Assess this cell for malaria.
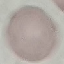
It is uninfected.

image_type: automatically extracted cell patch, resized to 64 × 64 pixels
preparation: thin blood film
capture: smartphone through the microscope eyepiece
stain: Giemsa